Report the malaria status of this cell.
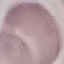
It is uninfected.

Cell patch, automatically extracted from a larger field of view and resized to 64 × 64 pixels. Giemsa-stained preparation. Thin blood film. Acquired by smartphone through the microscope eyepiece.